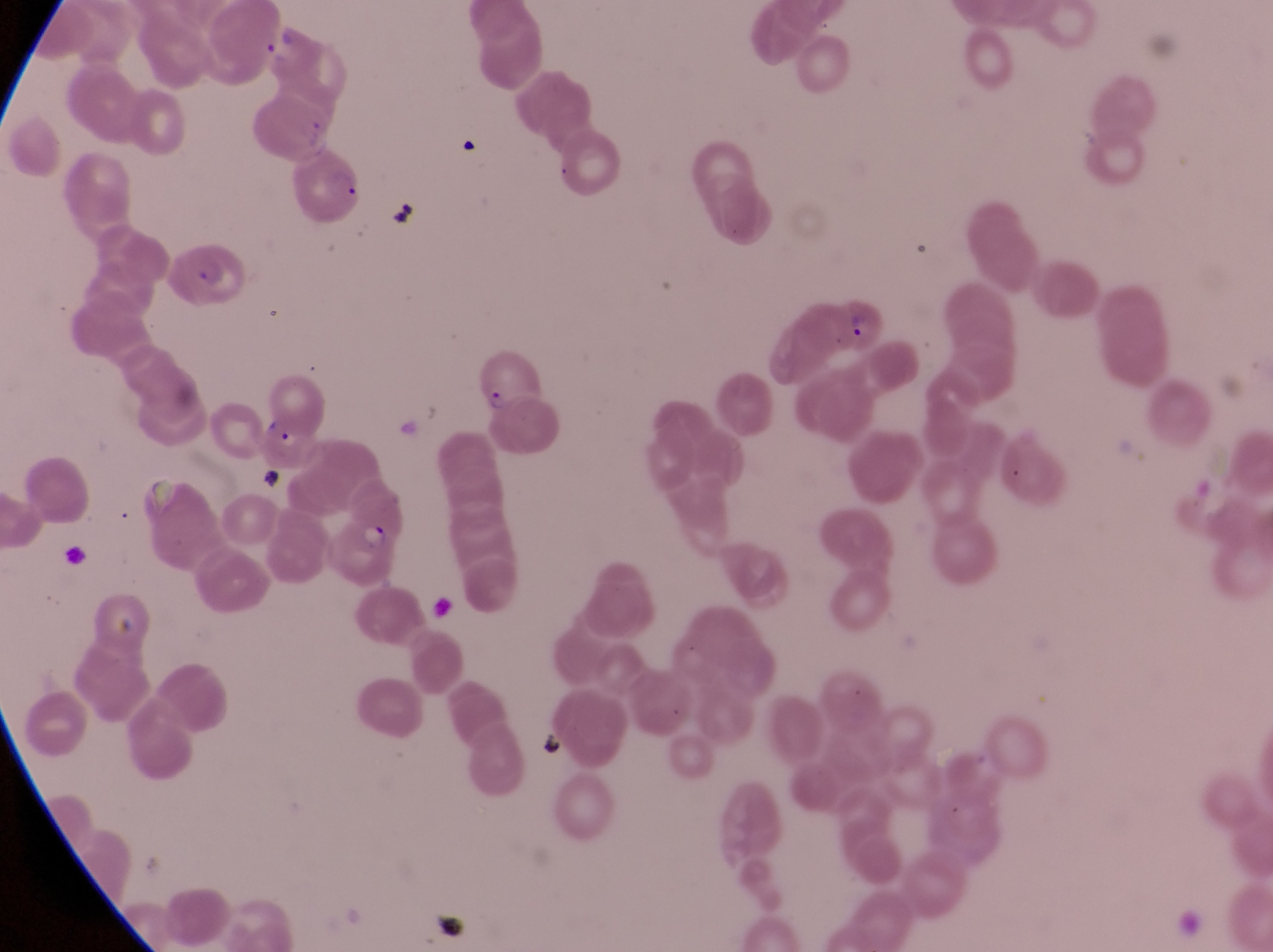
{
  "preparation": "thin blood film",
  "parasitised_red_blood_cell_locations": "approximate bounding boxes as left top right bottom in pixels: 299 150 368 218; 162 240 244 305; 831 295 886 357; 477 337 540 415; 262 415 322 472; 329 512 399 589",
  "field_of_view": "single",
  "trophozoite_locations": "approximate bounding boxes as left top right bottom in pixels: 258 34 303 67",
  "artifact_platelet_like_body_stain_precipitate_or_debris_locations": "approximate bounding boxes as left top right bottom in pixels: 392 193 424 230; 534 724 569 763",
  "image_size": "1273×952 pixels",
  "country": "Uganda",
  "magnification": "1000x",
  "capture": "smartphone photograph through the eyepiece of an Olympus CX-23 microscope"
}